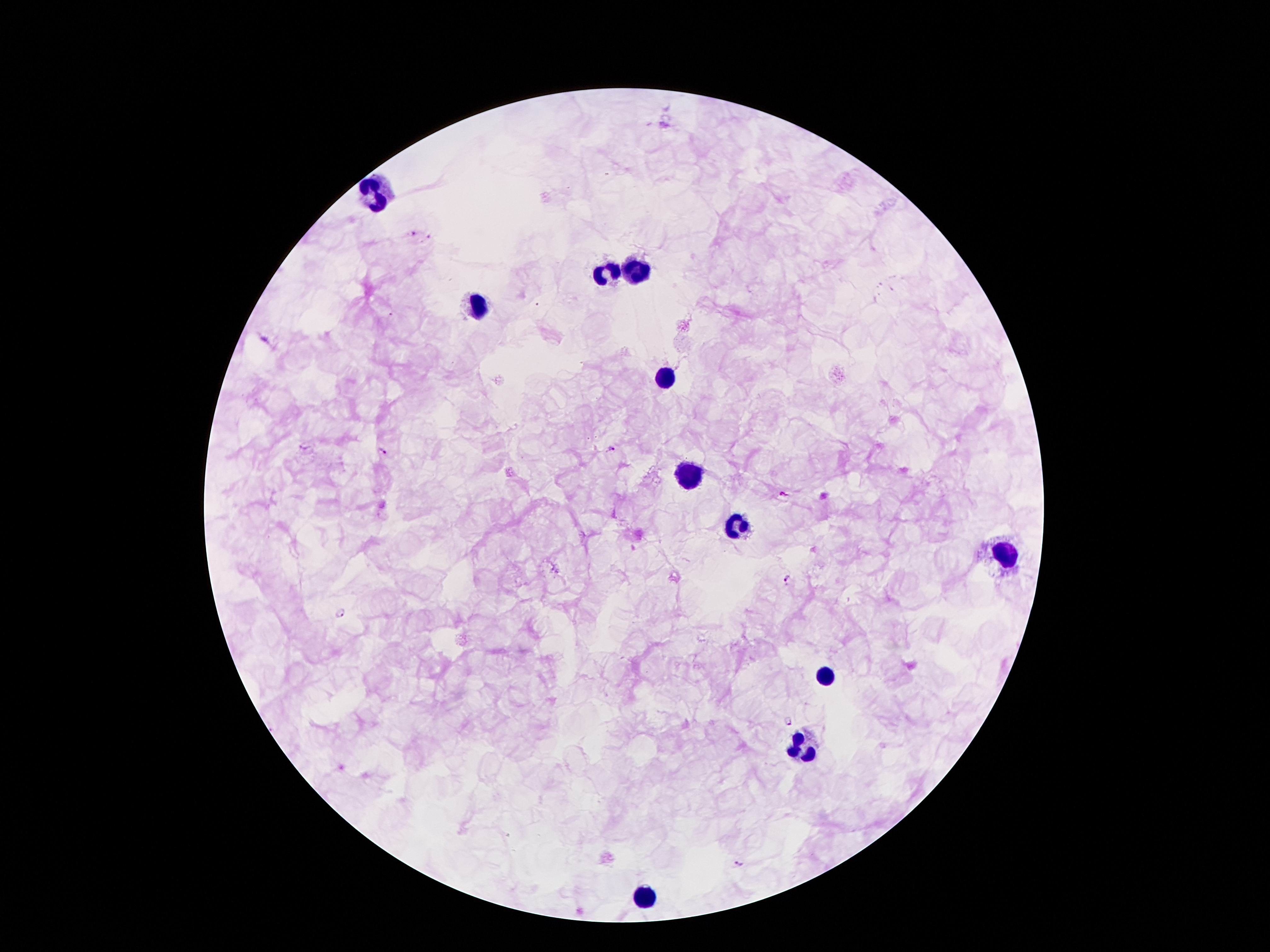
Approximate centers as (x, y) in pixels. Malaria parasite locations: (413, 233), (612, 448), (382, 451), (782, 494), (787, 580), (338, 615), (789, 721), (738, 865). Leukocyte locations: (375, 190), (634, 269), (607, 271), (476, 309), (663, 375), (689, 473), (739, 526), (1008, 555), (830, 675), (805, 749), (643, 897). 100x magnification. One field from this slide. Thick blood smear. Smartphone photograph taken through the microscope eyepiece. Image is 1270×952 pixels. Giemsa-stained preparation. Patient malaria status: infected with Plasmodium falciparum.